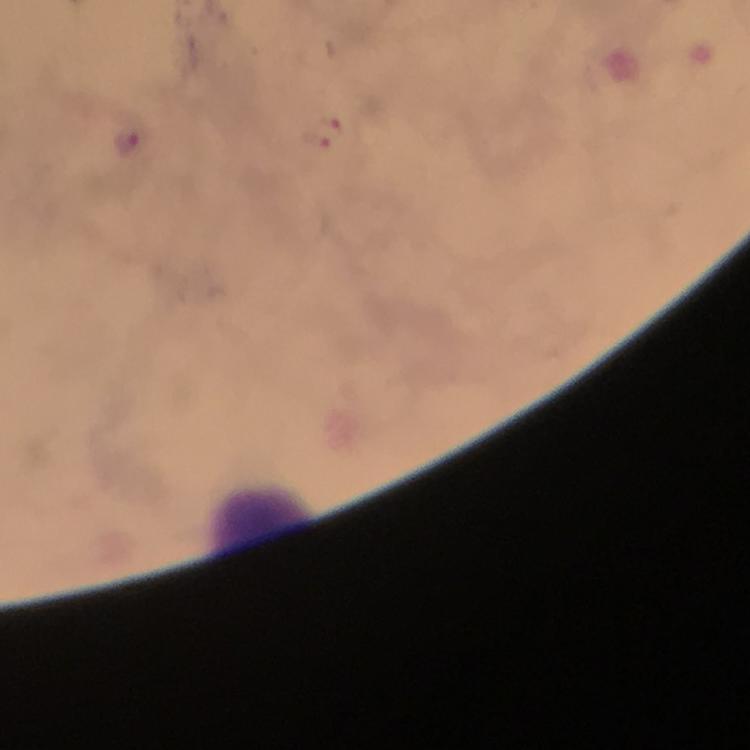

Approximate object centers, in pixels from the top-left corner.
Summary:
  - Malaria parasite locations: (x=128, y=141)
  - Image size: 750×750 pixels
  - Stain: Giemsa
  - Capture: smartphone camera through the microscope
  - Context: from a malaria diagnostic workup
  - Magnification: 100x
  - Preparation: thick blood smear
  - Cropped from: a single field of view
  - Immersion oil: applied